Give the preparation type.
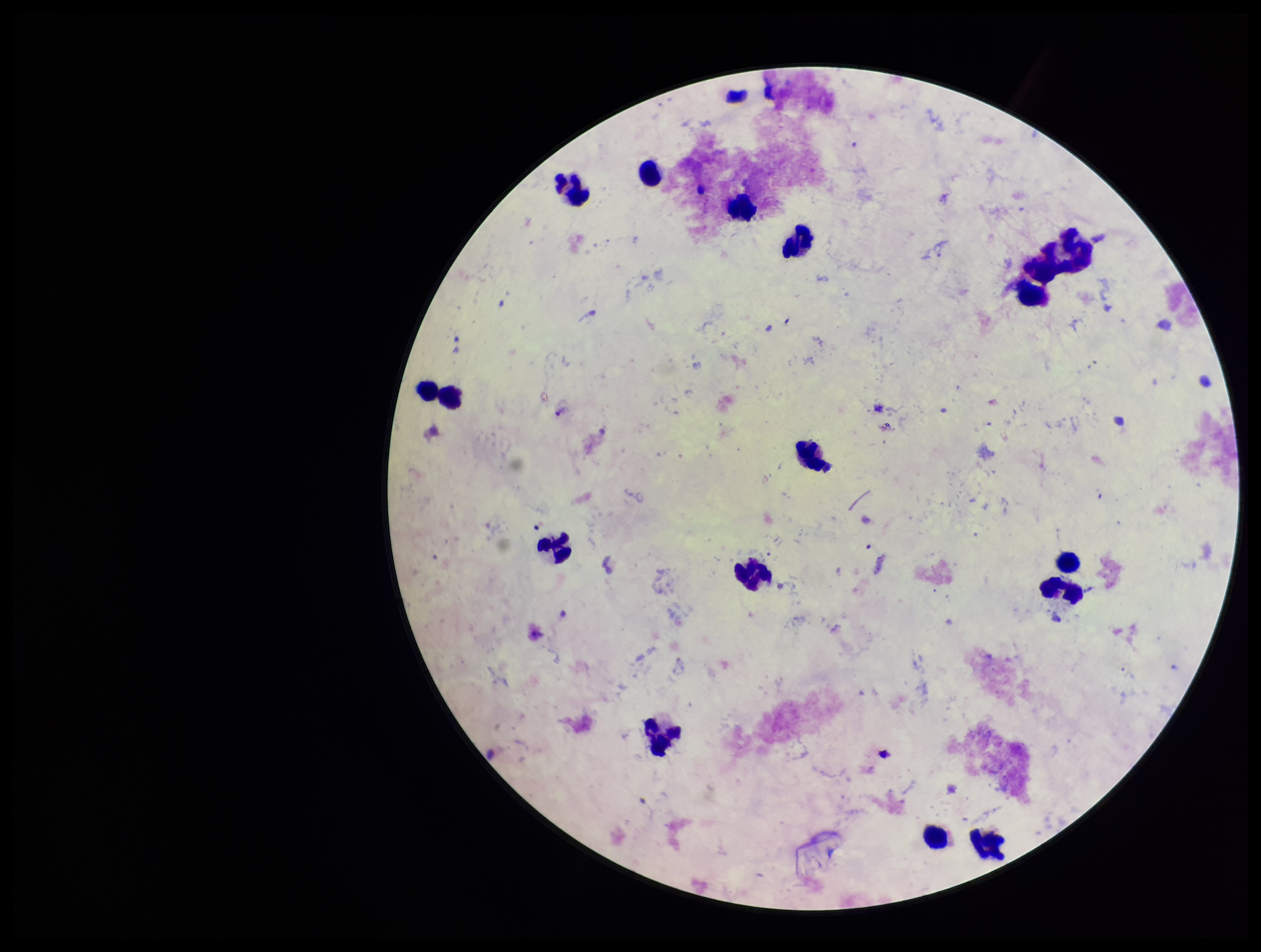

Thick.

Summary:
  - Parasite count: 0
  - Patient malaria status: negative
  - Field of view: one from this slide
  - Image size: 1261×952 pixels
  - Plasmodium parasites: none identified
  - Capture: smartphone photograph through the microscope eyepiece
  - Leukocyte count: 16
  - Stain: Giemsa